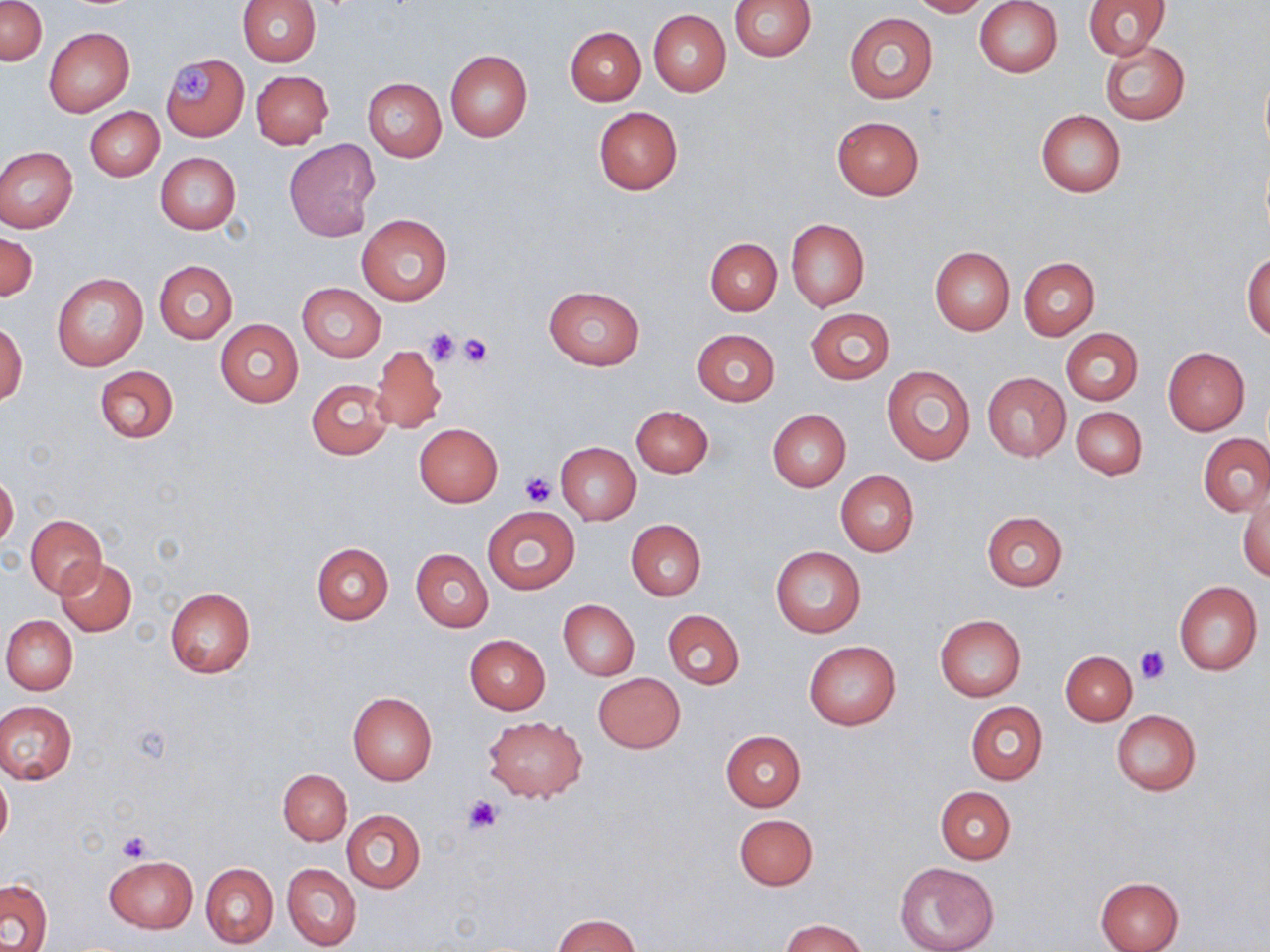
slide-level diagnosis = negative for blood parasites
preparation = thin blood film
magnification = 1000x
uninfected red blood cell locations = approximate bounding boxes as named x1/y1/x2/y2 corners in pixels: (x1=1, y1=0, x2=46, y2=66), (x1=237, y1=0, x2=322, y2=65), (x1=730, y1=0, x2=817, y2=61), (x1=908, y1=0, x2=989, y2=17), (x1=975, y1=0, x2=1063, y2=77), (x1=1083, y1=0, x2=1171, y2=59), (x1=648, y1=10, x2=731, y2=96), (x1=844, y1=13, x2=938, y2=103), (x1=44, y1=27, x2=135, y2=116), (x1=566, y1=27, x2=645, y2=105), (x1=1100, y1=41, x2=1190, y2=124), (x1=445, y1=50, x2=533, y2=141), (x1=162, y1=55, x2=248, y2=142), (x1=1260, y1=67, x2=1270, y2=158), (x1=251, y1=70, x2=333, y2=149), (x1=361, y1=77, x2=447, y2=162), (x1=85, y1=107, x2=164, y2=181), (x1=593, y1=107, x2=682, y2=195), (x1=1035, y1=110, x2=1126, y2=197), (x1=832, y1=117, x2=924, y2=199), (x1=284, y1=139, x2=378, y2=240), (x1=0, y1=145, x2=77, y2=233), (x1=155, y1=152, x2=240, y2=235), (x1=357, y1=214, x2=452, y2=304), (x1=786, y1=218, x2=869, y2=312), (x1=1, y1=229, x2=37, y2=302), (x1=705, y1=238, x2=782, y2=315), (x1=930, y1=247, x2=1014, y2=334), (x1=1242, y1=252, x2=1270, y2=339), (x1=1019, y1=257, x2=1100, y2=340), (x1=154, y1=260, x2=237, y2=344), (x1=51, y1=272, x2=148, y2=371), (x1=298, y1=283, x2=385, y2=361), (x1=544, y1=285, x2=646, y2=370), (x1=806, y1=308, x2=895, y2=384), (x1=215, y1=319, x2=303, y2=407), (x1=1, y1=321, x2=27, y2=404), (x1=1061, y1=328, x2=1143, y2=405), (x1=691, y1=329, x2=779, y2=406), (x1=371, y1=345, x2=446, y2=433), (x1=1163, y1=348, x2=1250, y2=435), (x1=95, y1=365, x2=179, y2=443), (x1=881, y1=366, x2=976, y2=466), (x1=982, y1=371, x2=1071, y2=461), (x1=305, y1=378, x2=394, y2=459), (x1=1071, y1=405, x2=1147, y2=479), (x1=632, y1=406, x2=713, y2=477), (x1=766, y1=409, x2=851, y2=491), (x1=414, y1=423, x2=503, y2=507), (x1=1199, y1=434, x2=1270, y2=516), (x1=555, y1=442, x2=641, y2=524), (x1=836, y1=471, x2=919, y2=556), (x1=0, y1=474, x2=19, y2=549), (x1=1240, y1=490, x2=1270, y2=581), (x1=483, y1=506, x2=580, y2=595), (x1=982, y1=511, x2=1068, y2=591), (x1=27, y1=514, x2=106, y2=597), (x1=625, y1=520, x2=706, y2=600), (x1=311, y1=541, x2=393, y2=625), (x1=770, y1=546, x2=867, y2=637), (x1=412, y1=549, x2=492, y2=632), (x1=54, y1=558, x2=136, y2=636), (x1=1174, y1=581, x2=1262, y2=675), (x1=165, y1=588, x2=256, y2=678), (x1=558, y1=599, x2=639, y2=680), (x1=663, y1=610, x2=744, y2=689), (x1=2, y1=615, x2=77, y2=695), (x1=935, y1=615, x2=1026, y2=700), (x1=464, y1=634, x2=551, y2=714), (x1=804, y1=641, x2=902, y2=731), (x1=1060, y1=651, x2=1137, y2=725), (x1=593, y1=672, x2=685, y2=753), (x1=348, y1=692, x2=437, y2=785), (x1=1, y1=701, x2=77, y2=784), (x1=967, y1=701, x2=1047, y2=784), (x1=1111, y1=710, x2=1200, y2=795), (x1=482, y1=715, x2=588, y2=803), (x1=721, y1=731, x2=806, y2=812), (x1=0, y1=768, x2=12, y2=849), (x1=278, y1=769, x2=351, y2=844), (x1=935, y1=787, x2=1015, y2=863), (x1=341, y1=809, x2=425, y2=893), (x1=733, y1=813, x2=818, y2=890), (x1=103, y1=854, x2=198, y2=933), (x1=201, y1=862, x2=278, y2=948), (x1=894, y1=862, x2=999, y2=952), (x1=282, y1=863, x2=361, y2=950), (x1=1094, y1=876, x2=1184, y2=952), (x1=1, y1=877, x2=54, y2=952), (x1=551, y1=914, x2=644, y2=952), (x1=781, y1=919, x2=868, y2=952)
stain = May-Grünwald-Giemsa
image size = 1270×952 pixels
platelet locations = approximate bounding boxes as named x1/y1/x2/y2 corners in pixels: (x1=169, y1=64, x2=217, y2=106), (x1=423, y1=327, x2=461, y2=367), (x1=458, y1=332, x2=493, y2=368), (x1=519, y1=472, x2=555, y2=506), (x1=1137, y1=646, x2=1169, y2=683), (x1=464, y1=796, x2=502, y2=833), (x1=117, y1=831, x2=155, y2=861)
field of view = one of a larger specimen
modality = optical microscopy